Comment on the morphology of the erythrocytes.
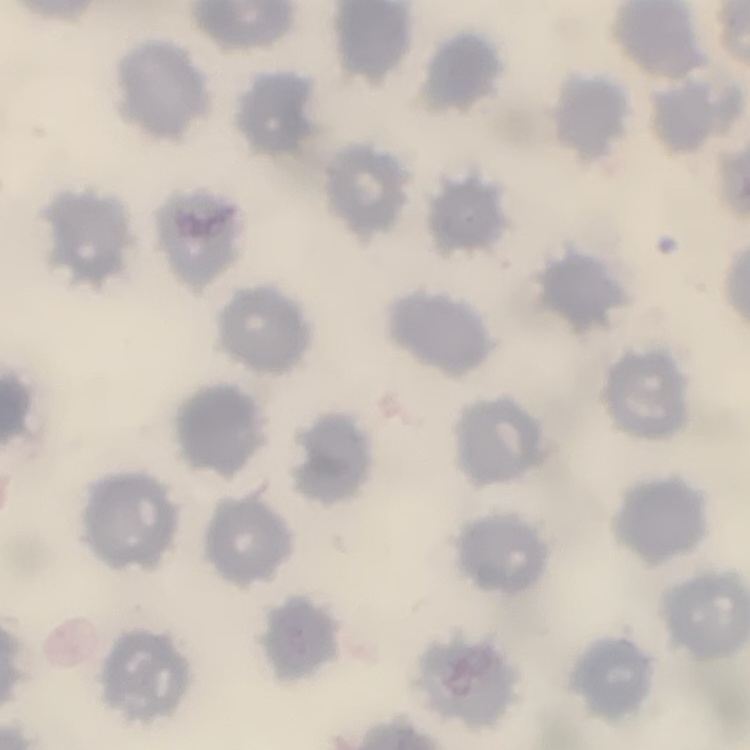
No rouleaux formation.

Square crop of a larger photomicrograph. Thin blood film. Field's or Giemsa stain.